Locate and identify every blood parasite.
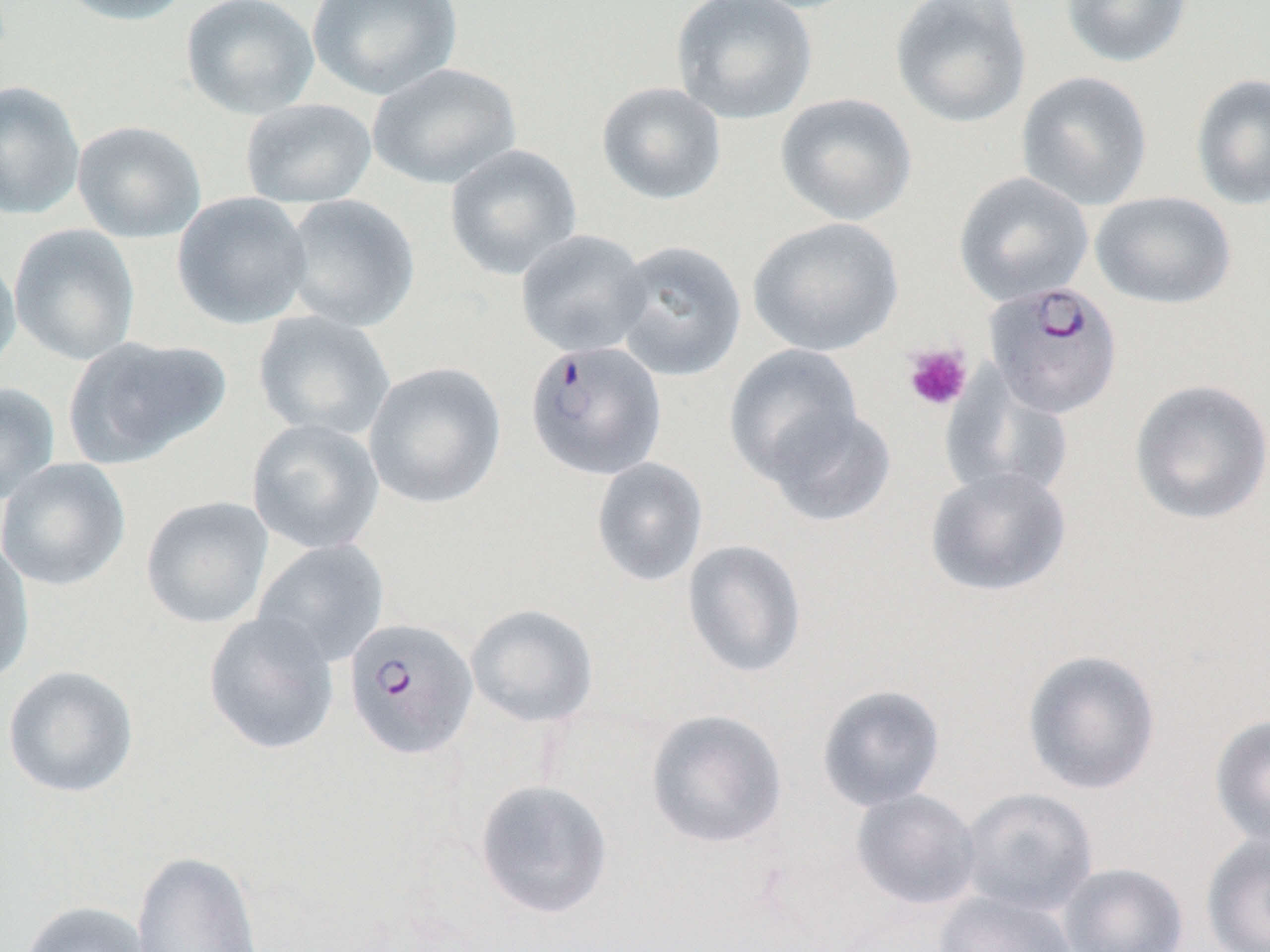
Approximate bounding boxes as (x1, y1, x2, y2) in pixels.
Plasmodium falciparum-infected red blood cells: (983, 281, 1123, 418), (524, 340, 668, 480), (343, 617, 478, 759).
No Plasmodium ovale, Plasmodium malariae, Plasmodium vivax, Babesia divergens, or Trypanosoma brucei observed.

slide_level_diagnosis: Plasmodium falciparum
field_of_view: one of a larger specimen
magnification: 1000x
platelet_locations: 'approximate bounding boxes as (x1, y1, x2, y2) in pixels: (902, 343, 973, 412)'
modality: light microscopy
preparation: thin blood film
image_size: 1270×952 pixels
uninfected_red_blood_cell_locations: 'approximate bounding boxes as (x1, y1, x2, y2) in pixels: (53, 0, 193, 26), (181, 0, 319, 120), (306, 0, 463, 101), (671, 0, 818, 125), (889, 0, 1033, 129), (1060, 0, 1194, 68), (367, 62, 521, 190), (1016, 70, 1153, 210), (1190, 73, 1270, 211), (0, 80, 86, 221), (596, 82, 727, 205), (775, 93, 917, 226), (240, 98, 377, 208), (71, 119, 206, 243), (444, 144, 583, 281), (953, 172, 1094, 306), (1091, 191, 1237, 310), (172, 192, 312, 329), (281, 194, 420, 332), (747, 217, 904, 357), (8, 224, 141, 366), (515, 229, 652, 357), (611, 239, 747, 381), (0, 249, 21, 379), (252, 310, 396, 441), (63, 335, 231, 468), (724, 343, 864, 485), (363, 361, 507, 509), (940, 370, 1075, 505), (1128, 379, 1270, 526), (0, 382, 60, 505), (763, 405, 897, 527), (246, 418, 385, 555), (591, 457, 709, 587), (0, 458, 131, 591), (925, 466, 1072, 598), (140, 495, 273, 630), (0, 537, 35, 687), (252, 539, 390, 668), (682, 539, 808, 679), (466, 604, 599, 728), (203, 610, 340, 755), (1021, 649, 1162, 795), (2, 664, 140, 798), (816, 684, 946, 811), (645, 709, 788, 850), (1209, 714, 1270, 849), (474, 779, 613, 919), (959, 787, 1098, 916), (851, 788, 982, 911), (1201, 831, 1270, 952), (131, 849, 264, 952), (1057, 862, 1189, 952), (933, 890, 1078, 952), (19, 900, 155, 952)'